Comment on the morphology of the red blood cells.
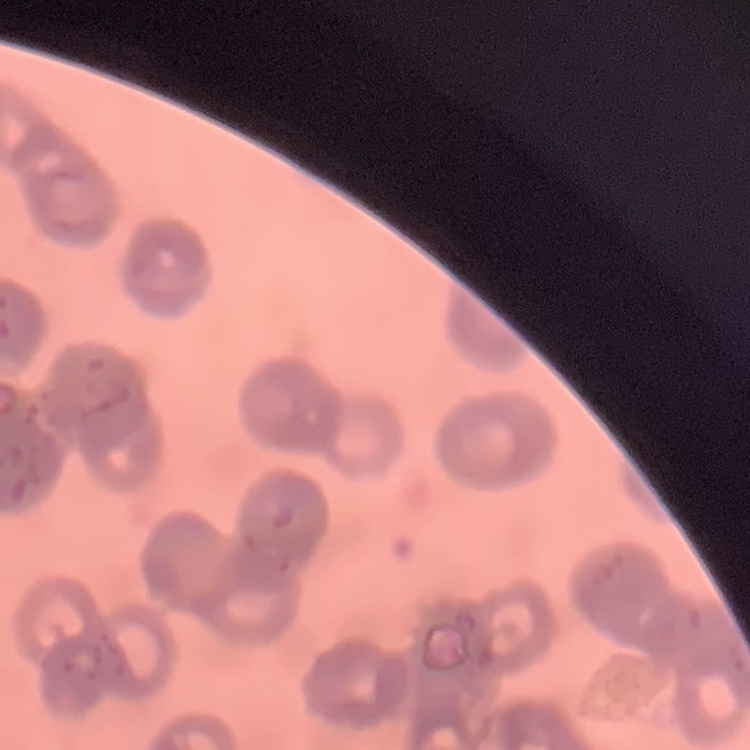
Rouleaux formation.

Summary:
  - Preparation: thin peripheral smear
  - Image type: one tile cut from a larger photomicrograph
  - Stain: Field's or Giemsa